State which parasite is depicted.
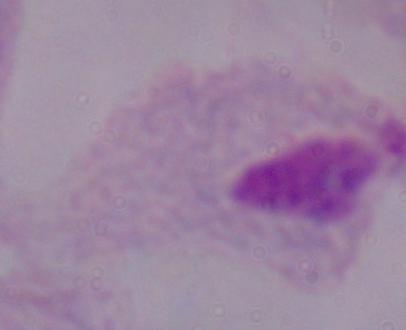
A trichomonad.

Micrograph. Captured at 1000x magnification.